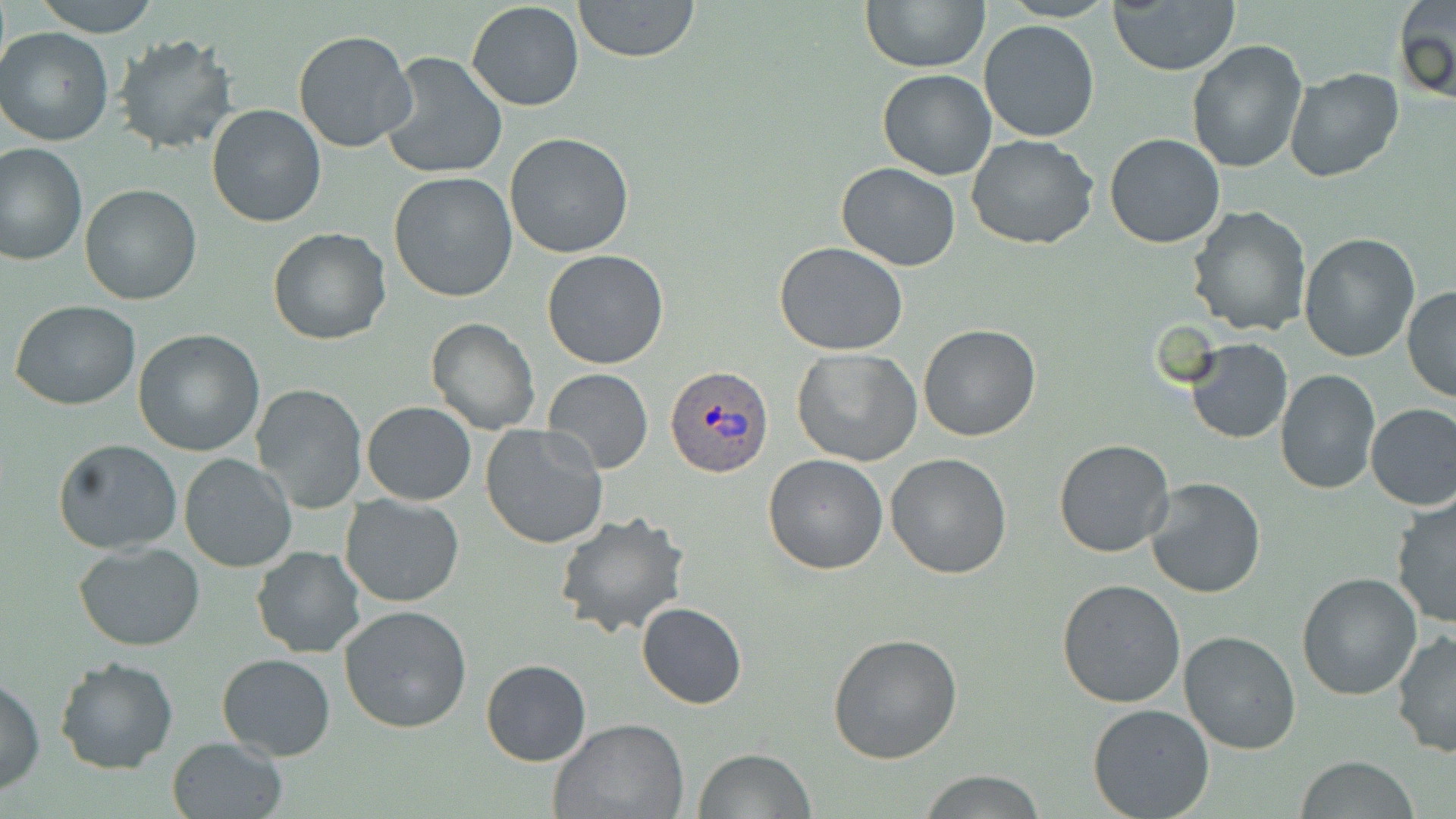

Summary:
  - Coordinate format: approximate bounding boxes as (x1, y1, x2, y2) in pixels
  - Uninfected red blood cell locations: (34, 0, 159, 36), (572, 0, 701, 63), (861, 0, 989, 72), (465, 1, 585, 112), (1109, 1, 1239, 75), (1394, 1, 1455, 105), (978, 20, 1099, 142), (1, 26, 117, 147), (293, 29, 419, 154), (113, 33, 236, 154), (1185, 39, 1307, 174), (379, 51, 509, 178), (1283, 67, 1404, 184), (878, 68, 997, 180), (207, 103, 326, 228), (1104, 131, 1225, 248), (504, 132, 634, 259), (966, 134, 1099, 249), (0, 143, 88, 265), (835, 162, 961, 271), (388, 171, 518, 303), (799, 177, 955, 345), (79, 183, 202, 303), (1186, 205, 1312, 337), (267, 227, 393, 345), (1297, 231, 1421, 361), (774, 240, 908, 355), (542, 248, 670, 369), (1401, 286, 1456, 403), (10, 300, 141, 411), (425, 318, 541, 437), (917, 324, 1041, 442), (133, 328, 265, 456), (1187, 339, 1292, 444), (791, 348, 922, 466), (541, 368, 652, 475), (1274, 369, 1381, 495), (250, 383, 367, 512), (362, 401, 477, 505), (1365, 402, 1456, 511), (479, 422, 608, 550), (52, 438, 184, 552), (1053, 438, 1175, 558), (885, 452, 1012, 578), (178, 453, 300, 573), (762, 453, 889, 574), (1146, 476, 1266, 599), (341, 492, 464, 606), (1389, 495, 1456, 631), (553, 511, 690, 638), (73, 543, 205, 651), (250, 546, 368, 660), (1296, 570, 1422, 701), (1056, 577, 1186, 706), (638, 602, 747, 709), (339, 604, 474, 735), (1178, 630, 1302, 754), (1391, 630, 1456, 757), (827, 631, 963, 763), (216, 652, 335, 760), (55, 655, 179, 773), (481, 658, 591, 766), (1, 674, 46, 795), (1087, 704, 1215, 818), (549, 718, 690, 819), (165, 737, 288, 819), (694, 748, 814, 818), (1295, 757, 1421, 818), (916, 770, 1050, 818)
  - Plasmodium ovale-infected red blood cell locations: (664, 364, 770, 477)
  - Slide-level diagnosis: Plasmodium ovale
  - Preparation: thin blood smear
  - Magnification: 1000x
  - Field of view: single
  - Modality: light microscopy
  - Stain: May-Grünwald-Giemsa
  - Image size: 1456×819 pixels